Locate every blood parasite and identify its species.
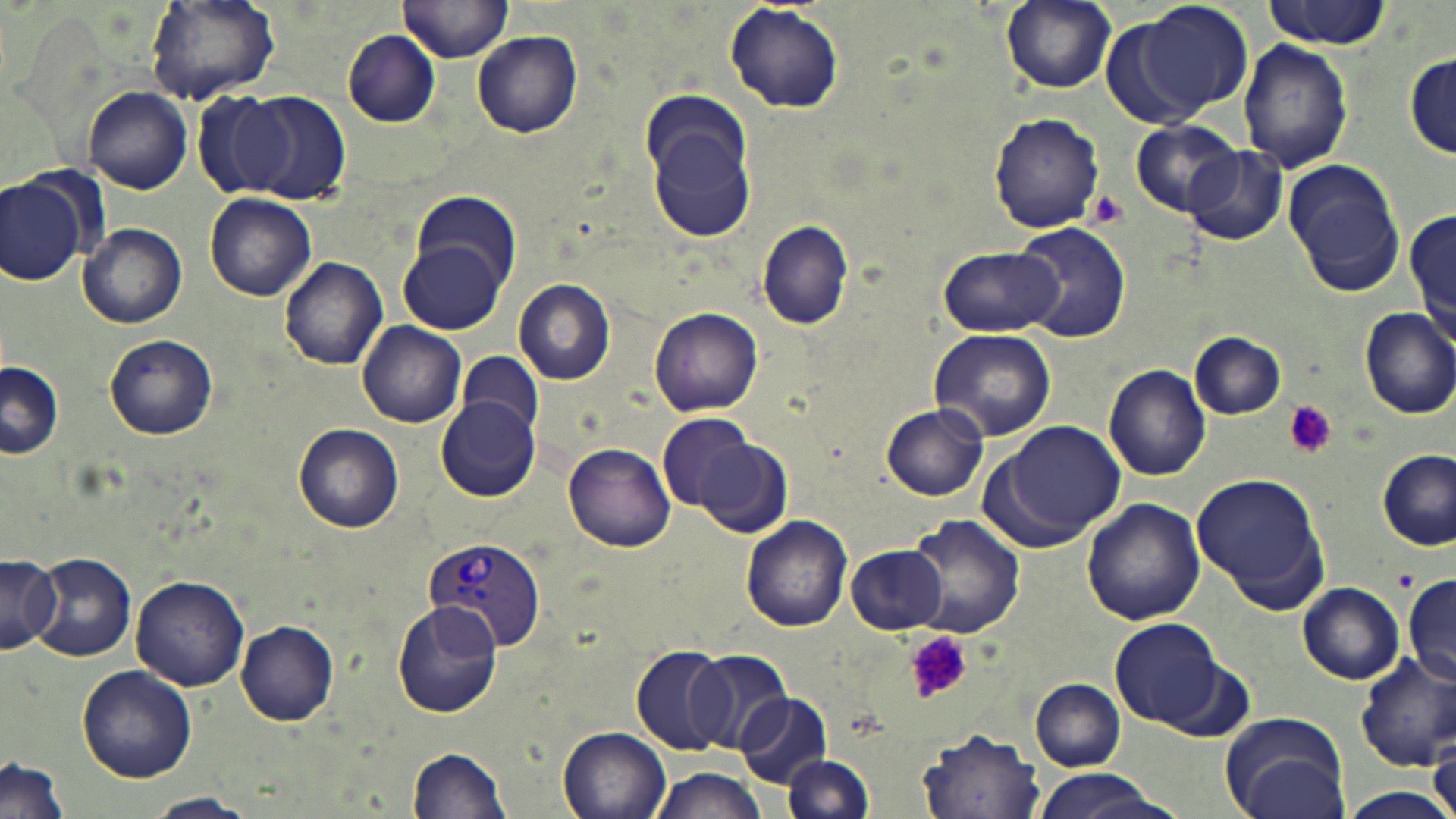

Approximate bounding boxes as [x1, y1, x2, y2] in pixels.
Plasmodium vivax-infected red blood cells: [422, 537, 544, 655].
No Plasmodium falciparum, Plasmodium ovale, Plasmodium malariae, Babesia divergens, or Trypanosoma brucei observed.

Summary:
  - Uninfected red blood cell locations: [147, 0, 280, 106], [398, 0, 514, 62], [998, 0, 1120, 95], [1110, 0, 1253, 127], [1261, 1, 1390, 47], [723, 4, 845, 114], [343, 31, 442, 128], [472, 32, 583, 138], [1239, 39, 1354, 174], [1405, 51, 1454, 158], [82, 87, 191, 195], [191, 89, 297, 200], [244, 91, 351, 206], [646, 105, 758, 245], [989, 112, 1104, 234], [1131, 120, 1242, 216], [1185, 147, 1286, 244], [1283, 160, 1407, 297], [0, 176, 84, 284], [409, 192, 522, 293], [205, 194, 316, 303], [1408, 205, 1455, 341], [757, 220, 854, 331], [1014, 222, 1130, 342], [80, 223, 187, 328], [399, 241, 506, 332], [939, 245, 1060, 337], [279, 256, 388, 369], [514, 280, 616, 385], [648, 305, 763, 417], [1360, 307, 1456, 417], [358, 322, 467, 428], [927, 328, 1057, 441], [1190, 332, 1287, 419], [104, 333, 217, 440], [458, 350, 544, 439], [0, 362, 63, 460], [1103, 363, 1211, 481], [435, 398, 539, 501], [881, 404, 989, 501], [656, 411, 759, 513], [1000, 421, 1127, 538], [294, 423, 405, 532], [698, 436, 792, 540], [564, 442, 677, 551], [1378, 450, 1455, 549], [1193, 472, 1328, 608], [1082, 498, 1206, 626], [907, 514, 1026, 639], [741, 515, 852, 632], [845, 543, 949, 635], [31, 551, 136, 662], [0, 553, 62, 653], [1404, 575, 1456, 688], [131, 576, 249, 691], [1297, 582, 1406, 685], [390, 602, 503, 719], [1108, 618, 1227, 730], [237, 620, 340, 725], [630, 647, 730, 756], [688, 651, 794, 752], [1354, 654, 1456, 771], [77, 665, 198, 784], [1031, 679, 1126, 772], [737, 692, 831, 788], [1217, 710, 1352, 819], [558, 727, 672, 819], [917, 728, 1045, 818], [1428, 735, 1455, 819], [407, 747, 512, 818], [783, 754, 874, 818], [1, 755, 71, 819], [645, 767, 769, 819], [1027, 767, 1176, 819], [1336, 787, 1456, 818], [147, 793, 257, 818]
  - Platelet locations: [1085, 191, 1128, 228], [1282, 401, 1341, 460], [1394, 567, 1418, 592], [906, 630, 973, 706]
  - Slide-level diagnosis: Plasmodium vivax
  - Magnification: 1000x
  - Stain: May-Grünwald-Giemsa
  - Field of view: one of a larger specimen
  - Preparation: thin blood film
  - Modality: light microscopy
  - Image size: 1456×819 pixels